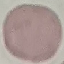
Summary:
  - Malaria status: uninfected
  - Capture: smartphone through the microscope eyepiece
  - Stain: Giemsa
  - Preparation: thin blood film
  - Image type: automatically extracted cell patch, resized to 64 × 64 pixels